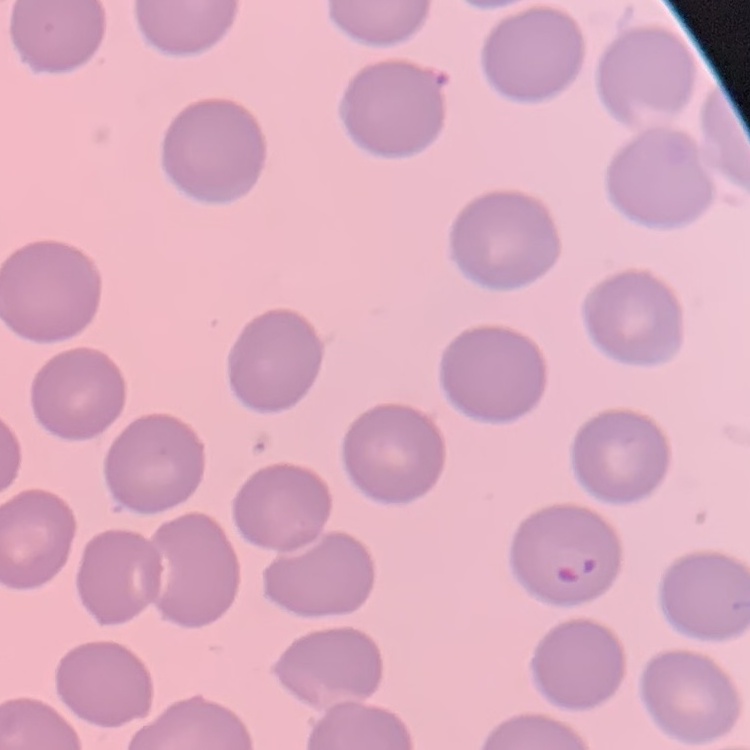

erythrocyte morphology = no rouleaux formation
preparation = thin blood smear
stain = Field's or Giemsa
image type = one tile cut from a larger photomicrograph